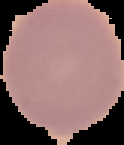

Summary:
  - Preparation: thin blood smear
  - Image size: 124×145 pixels
  - Result: no Plasmodium parasites seen
  - Image type: cell region segmented out of the field of view; surrounding area masked to black